Give the extent of all uninfected red blood cells.
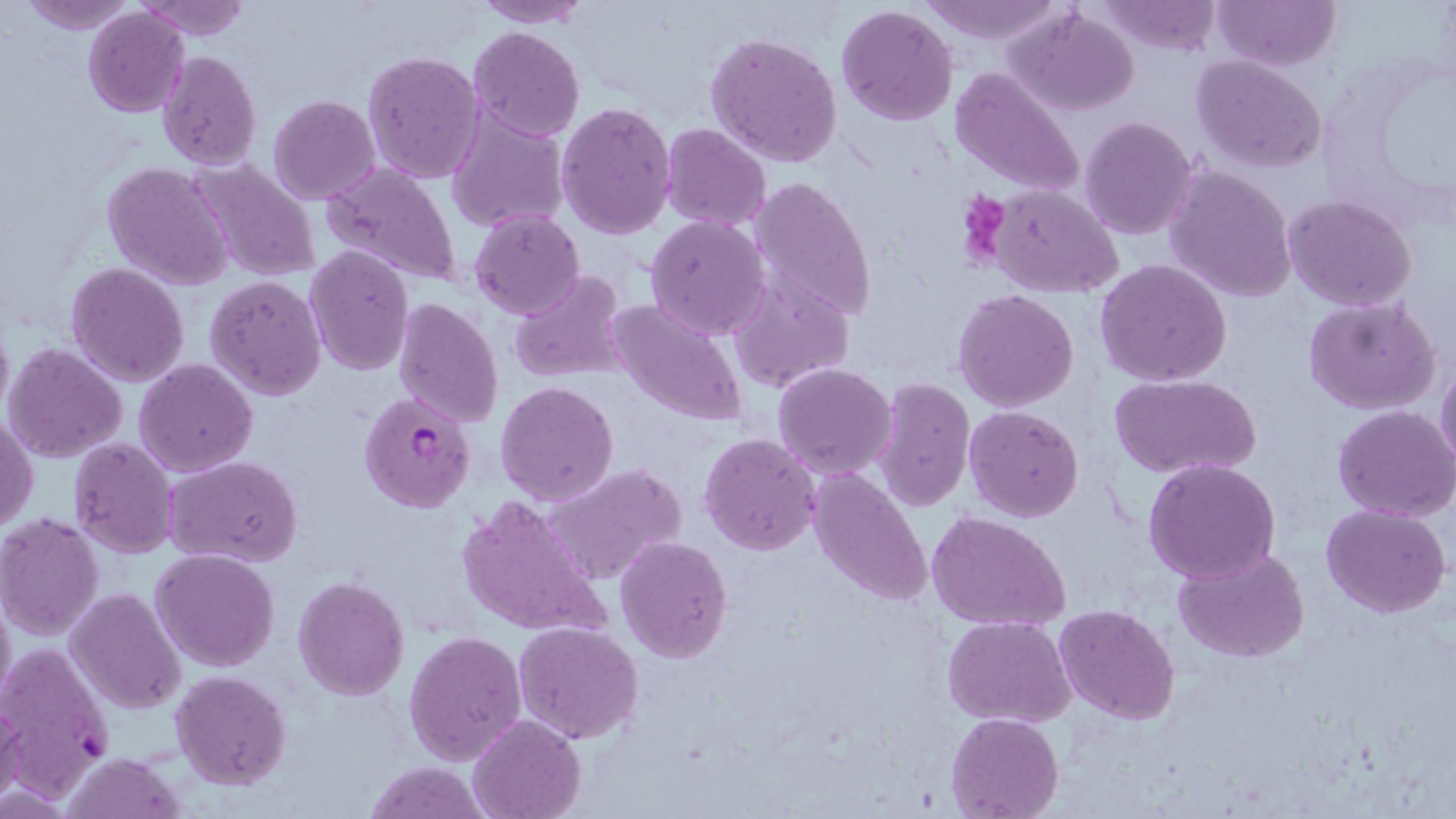
Approximate bounding boxes as (x1, y1, x2, y2) in pixels.
Uninfected red blood cells: (21, 0, 138, 33), (135, 0, 252, 41), (919, 0, 1067, 46), (1213, 0, 1340, 71), (471, 1, 590, 27), (1097, 1, 1221, 54), (836, 5, 960, 126), (81, 6, 190, 117), (1006, 6, 1141, 117), (468, 26, 584, 140), (706, 30, 843, 167), (157, 49, 262, 170), (362, 50, 485, 185), (1193, 54, 1328, 172), (949, 68, 1086, 200), (267, 94, 380, 205), (555, 100, 677, 239), (446, 109, 569, 236), (1079, 116, 1198, 240), (661, 123, 772, 233), (189, 157, 322, 282), (103, 162, 235, 291), (319, 162, 463, 288), (1164, 166, 1298, 302), (750, 175, 876, 323), (988, 183, 1123, 298), (1285, 193, 1418, 311), (470, 210, 585, 318), (645, 214, 771, 340), (304, 245, 413, 377), (1095, 260, 1233, 388), (66, 262, 191, 387), (509, 269, 628, 385), (204, 274, 327, 402), (730, 274, 855, 392), (951, 289, 1080, 412), (393, 296, 504, 428), (1302, 297, 1442, 415), (607, 298, 750, 428), (0, 312, 13, 424), (3, 342, 128, 463), (135, 358, 257, 476), (1437, 359, 1456, 478), (771, 362, 898, 482), (1111, 374, 1262, 480), (873, 377, 975, 511), (494, 380, 619, 505), (1333, 404, 1456, 520), (964, 406, 1085, 521), (1, 412, 39, 532), (698, 432, 821, 557), (67, 437, 178, 558), (166, 457, 302, 567), (1142, 459, 1282, 583), (540, 462, 686, 587), (806, 469, 934, 607), (457, 495, 608, 642), (1321, 503, 1452, 617), (926, 510, 1071, 633), (0, 514, 104, 638), (615, 534, 734, 663), (1174, 546, 1311, 663), (149, 549, 280, 672), (292, 575, 411, 700), (66, 587, 185, 715), (0, 591, 14, 708), (1053, 604, 1181, 724), (943, 614, 1077, 728), (512, 622, 643, 745), (404, 628, 528, 765), (0, 646, 115, 797), (171, 670, 291, 789), (0, 700, 26, 809), (945, 712, 1065, 819), (468, 714, 586, 819), (61, 752, 186, 819), (361, 759, 494, 818).

Plasmodium falciparum-infected red blood cell locations: (360, 390, 476, 513). Platelet locations: (958, 190, 1011, 257). Slide-level diagnosis: Plasmodium falciparum. Image is 1456×819 pixels. May-Grünwald-Giemsa-stained preparation. Thin blood film. 1000x magnification. Single field of view. Optical microscopy.